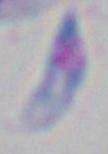
magnification = 1000x
identification = Toxoplasma gondii
modality = photomicrograph